Give the extent of all Plasmodium falciparum-infected red blood cells.
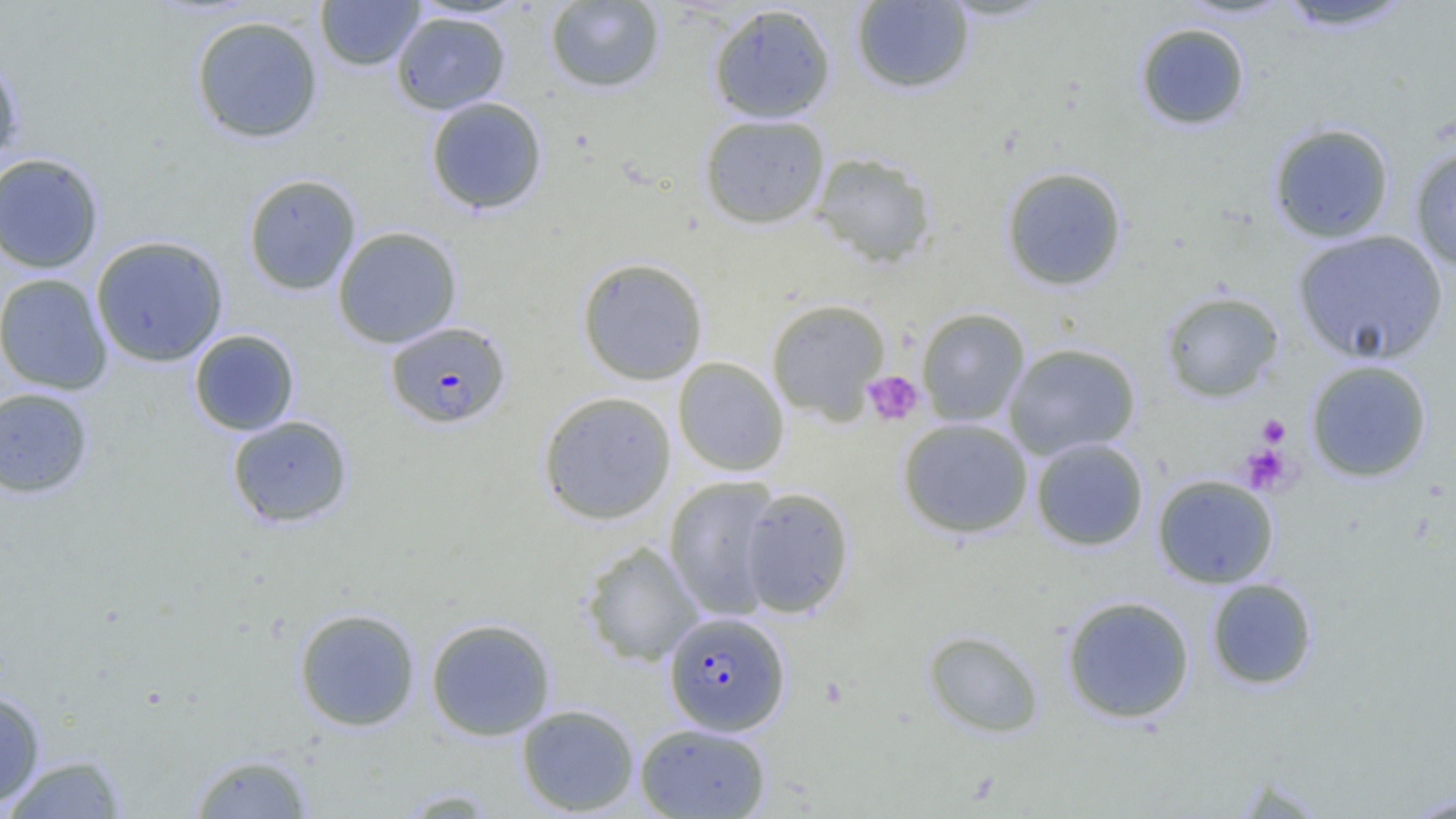

Approximate bounding boxes as named x1/y1/x2/y2 corners in pixels.
Plasmodium falciparum-infected red blood cells: (x1=385, y1=321, x2=511, y2=429), (x1=663, y1=611, x2=791, y2=736).

Summary:
  - Platelet locations: (x1=862, y1=371, x2=925, y2=426), (x1=1257, y1=415, x2=1290, y2=447), (x1=1241, y1=445, x2=1292, y2=495)
  - Uninfected red blood cell locations: (x1=315, y1=0, x2=423, y2=71), (x1=544, y1=1, x2=665, y2=93), (x1=850, y1=1, x2=975, y2=94), (x1=1274, y1=1, x2=1417, y2=33), (x1=708, y1=3, x2=837, y2=123), (x1=391, y1=11, x2=511, y2=114), (x1=190, y1=15, x2=324, y2=144), (x1=1135, y1=21, x2=1251, y2=131), (x1=0, y1=52, x2=24, y2=170), (x1=425, y1=96, x2=548, y2=215), (x1=699, y1=114, x2=830, y2=229), (x1=1268, y1=122, x2=1395, y2=243), (x1=1408, y1=144, x2=1456, y2=271), (x1=810, y1=151, x2=938, y2=270), (x1=0, y1=152, x2=104, y2=274), (x1=1000, y1=166, x2=1128, y2=291), (x1=243, y1=173, x2=361, y2=296), (x1=333, y1=226, x2=462, y2=348), (x1=1293, y1=230, x2=1447, y2=365), (x1=90, y1=235, x2=229, y2=367), (x1=576, y1=257, x2=709, y2=385), (x1=0, y1=273, x2=113, y2=394), (x1=1160, y1=291, x2=1285, y2=403), (x1=766, y1=299, x2=891, y2=423), (x1=916, y1=307, x2=1030, y2=427), (x1=189, y1=329, x2=300, y2=436), (x1=1003, y1=342, x2=1141, y2=459), (x1=672, y1=357, x2=789, y2=477), (x1=1305, y1=359, x2=1433, y2=483), (x1=0, y1=387, x2=94, y2=499), (x1=537, y1=391, x2=677, y2=524), (x1=226, y1=414, x2=354, y2=528), (x1=897, y1=417, x2=1033, y2=539), (x1=1031, y1=437, x2=1148, y2=551), (x1=663, y1=474, x2=782, y2=620), (x1=1151, y1=474, x2=1279, y2=589), (x1=739, y1=486, x2=855, y2=619), (x1=581, y1=540, x2=705, y2=667), (x1=1205, y1=577, x2=1318, y2=690), (x1=1061, y1=595, x2=1195, y2=724), (x1=293, y1=608, x2=421, y2=732), (x1=425, y1=618, x2=556, y2=741), (x1=923, y1=629, x2=1045, y2=738), (x1=0, y1=688, x2=46, y2=809), (x1=516, y1=703, x2=640, y2=816), (x1=634, y1=723, x2=772, y2=819), (x1=188, y1=751, x2=315, y2=818), (x1=1, y1=754, x2=130, y2=818), (x1=396, y1=788, x2=500, y2=817), (x1=1400, y1=791, x2=1456, y2=818)
  - Slide-level diagnosis: Plasmodium falciparum
  - Magnification: 1000x
  - Image size: 1456×819 pixels
  - Preparation: thin blood smear
  - Modality: optical microscopy
  - Field of view: one of a larger specimen